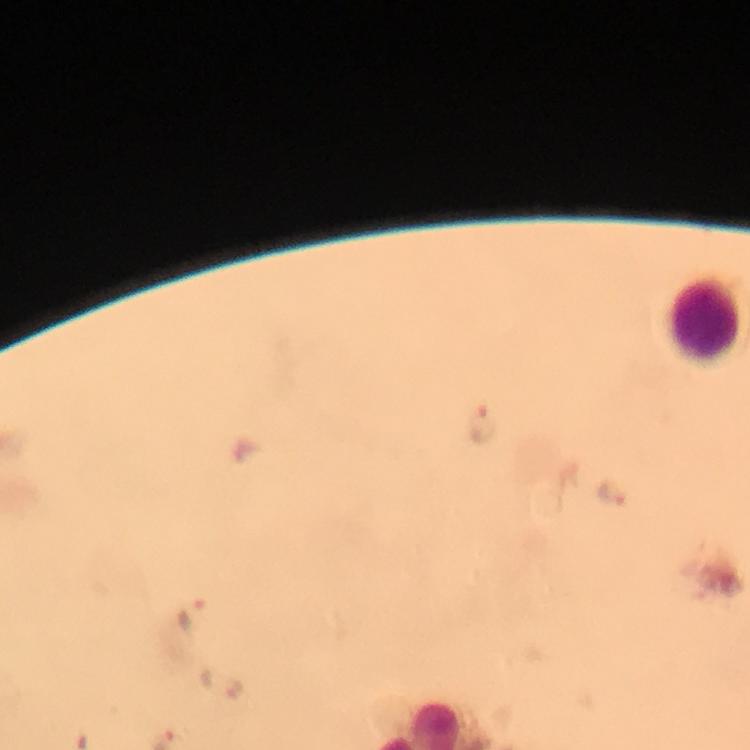 Approximate centers as [x, y] in pixels. Plasmodium parasite locations: [481, 427], [609, 489], [189, 614]. Leukocyte locations: [695, 318]. Photographed through the microscope with a smartphone camera. Thick blood film. 100x magnification. From a malaria diagnostic workup. Immersion oil was used. Image is 750×750 pixels. A crop from one field of view. Giemsa-stained preparation.